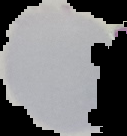
image size = 127×136 pixels
image type = cell region segmented out of the field of view; surrounding area masked to black
preparation = thin blood film
malaria status = uninfected